Describe the morphology of the red blood cells.
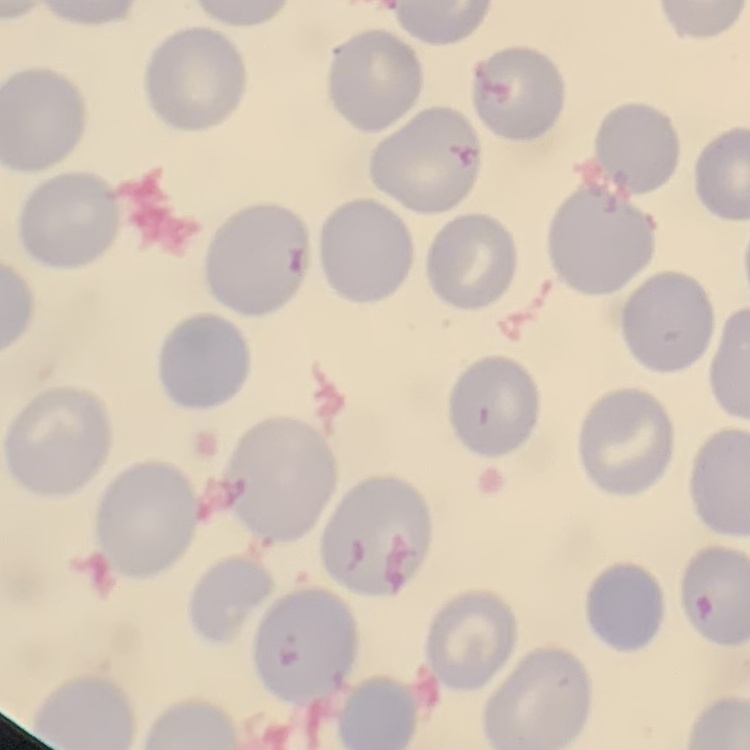

They show no rouleaux formation.

preparation = thin peripheral smear
image type = square crop of a larger photomicrograph
stain = Field's or Giemsa